State which cell type is depicted.
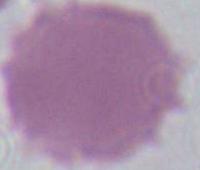
This is an erythrocyte.

magnification: 1000x
modality: photomicrograph